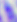
identification: Toxoplasma gondii
magnification: 400x
modality: photomicrograph